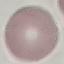
Summary:
  - Result: no malaria parasites detected
  - Stain: Giemsa
  - Image type: cell patch, automatically extracted from a larger field of view and resized to 64 × 64 pixels
  - Capture: smartphone camera at the microscope eyepiece
  - Preparation: thin smear